Identify the parasite.
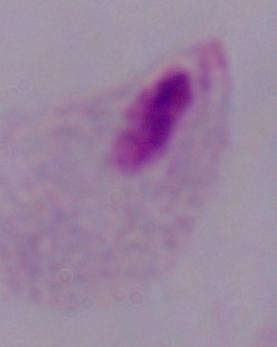

A trichomonad.

Micrograph. Captured at 1000x magnification.